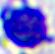 Captured at 400x magnification. A leukocyte is seen. Photomicrograph.